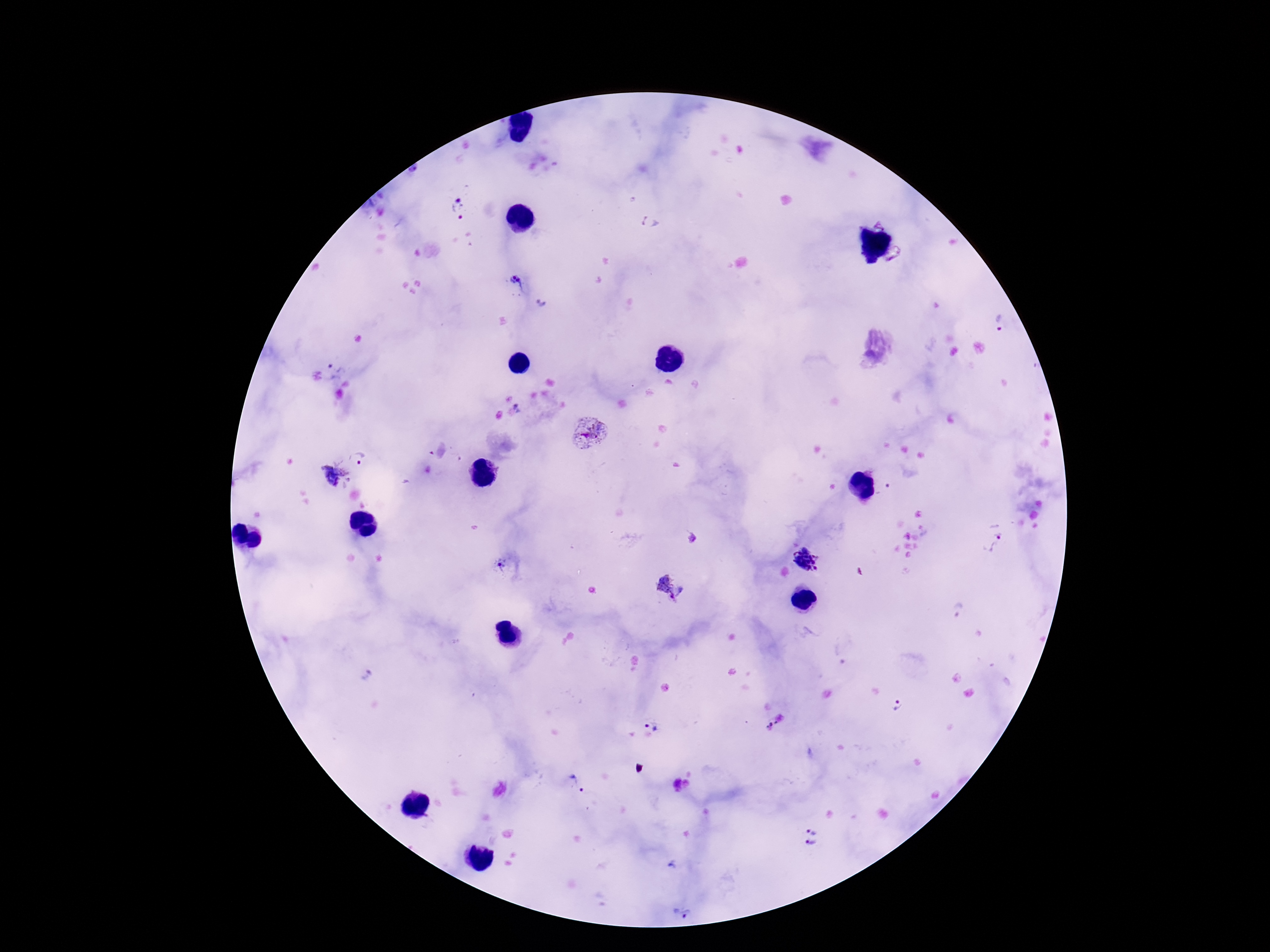

capture = smartphone camera through the microscope eyepiece
image size = 1270×952 pixels
patient malaria status = positive
stain = Giemsa
Plasmodium parasite locations = approximate centers as (x, y) in pixels: (460, 208), (880, 221), (651, 223), (897, 258), (517, 282), (541, 305), (1000, 326), (336, 367), (519, 407), (586, 434), (359, 456), (335, 474), (993, 537), (807, 559), (500, 565), (671, 587), (898, 707), (654, 719), (775, 722), (770, 724), (767, 726), (579, 781), (814, 827), (812, 844), (682, 913)
preparation = thick blood film
magnification = 100x
field of view = single